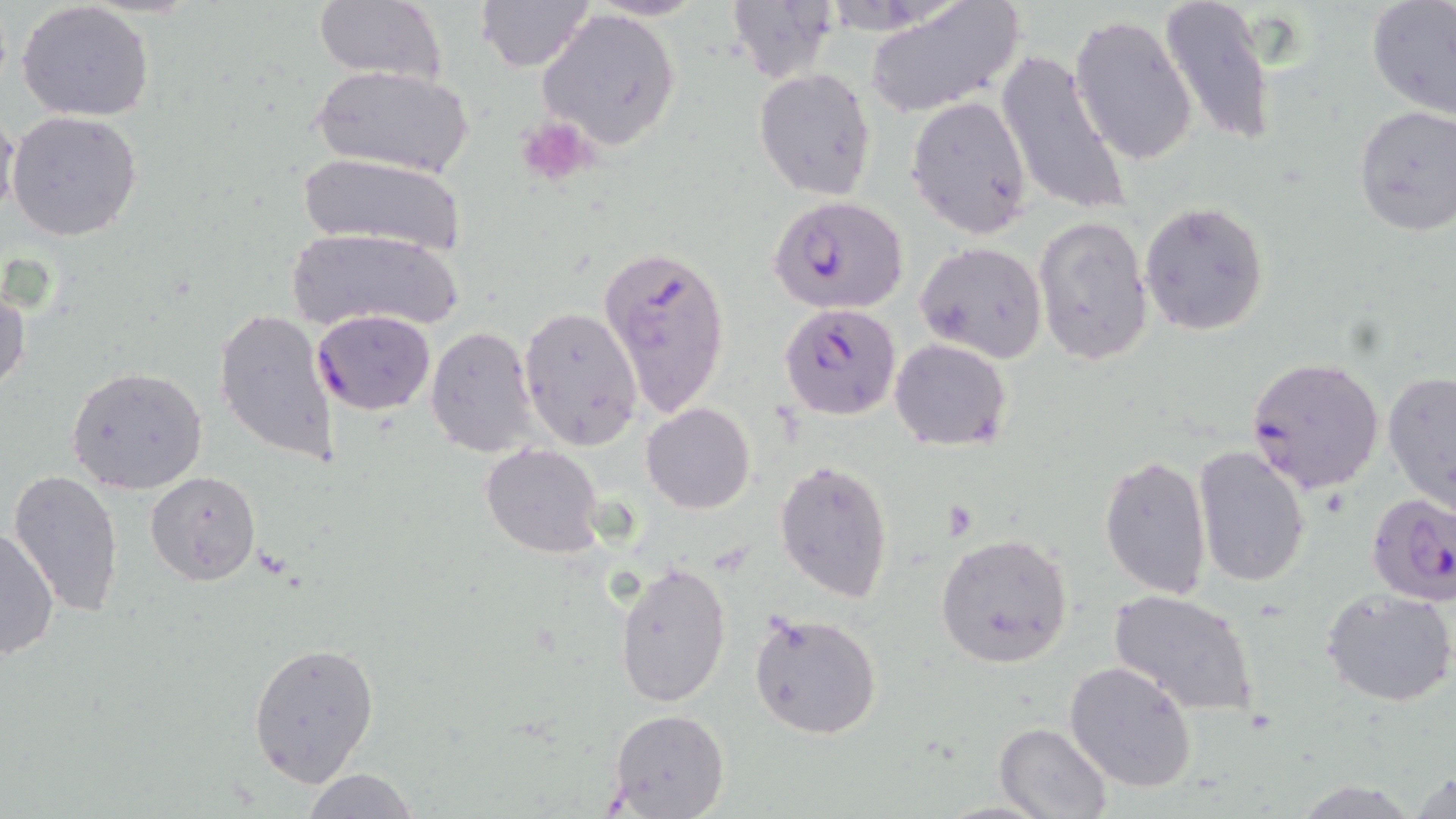
slide_level_diagnosis: Plasmodium falciparum
platelet_locations: 'approximate bounding boxes as (x1,y1)-(x2,y2) corner pairs in pixels: (515,115)-(598,189)'
modality: optical microscopy
stain: May-Grünwald-Giemsa
plasmodium_falciparum_infected_red_blood_cell_locations: 'approximate bounding boxes as (x1,y1)-(x2,y2) corner pairs in pixels: (768,194)-(909,314), (597,241)-(731,421), (778,301)-(904,421), (311,309)-(436,415), (1244,355)-(1385,495), (1365,492)-(1456,608)'
uninfected_red_blood_cell_locations: 'approximate bounding boxes as (x1,y1)-(x2,y2) corner pairs in pixels: (313,0)-(445,87), (727,0)-(839,80), (865,0)-(1025,117), (1160,0)-(1276,150), (476,1)-(594,73), (1365,1)-(1456,119), (15,2)-(155,122), (536,7)-(683,152), (1070,14)-(1198,167), (994,49)-(1133,220), (311,64)-(472,179), (754,68)-(878,200), (906,95)-(1033,237), (1352,105)-(1456,237), (5,110)-(143,242), (0,111)-(21,227), (296,152)-(468,258), (1140,201)-(1270,336), (1033,214)-(1154,368), (286,226)-(466,336), (915,240)-(1048,365), (0,280)-(30,398), (518,307)-(643,452), (213,308)-(340,464), (425,325)-(541,458), (888,338)-(1013,451), (64,365)-(209,496), (1382,370)-(1456,513), (641,402)-(757,513), (480,443)-(606,559), (1193,446)-(1311,588), (1100,454)-(1212,599), (774,459)-(896,604), (9,469)-(127,617), (146,469)-(263,588), (0,525)-(59,661), (935,532)-(1074,670), (615,560)-(732,707), (1323,588)-(1456,709), (1109,590)-(1258,718), (748,611)-(883,741), (248,641)-(379,785), (1064,660)-(1198,794), (607,709)-(729,819), (993,722)-(1112,819), (1410,766)-(1456,819), (300,768)-(420,819)'
magnification: 1000x
field_of_view: one of a larger specimen
image_size: 1456×819 pixels
preparation: thin blood film